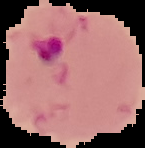
Segmented cell region on a black background. From a thin blood smear. Result: malaria parasites detected. Image is 145×148 pixels.